Report the malaria status of this cell.
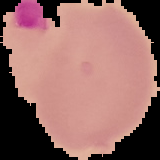
Uninfected.

Image is 160×160 pixels. The area outside the segmented cell region is set to black. From a thin blood smear.